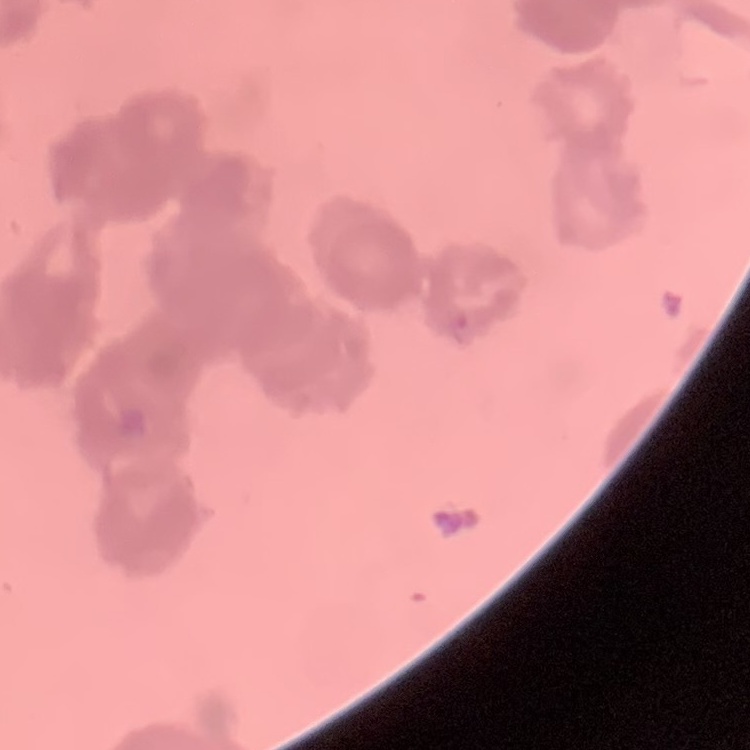
Summary:
  - Erythrocyte morphology: rouleaux formation
  - Stain: Field's or Giemsa
  - Image type: square crop of a larger photomicrograph
  - Preparation: thin blood film